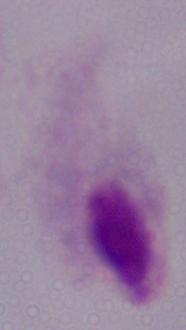

Summary:
  - Identification: trichomonad
  - Magnification: 1000x
  - Modality: micrograph